Identify the blood parasite species.
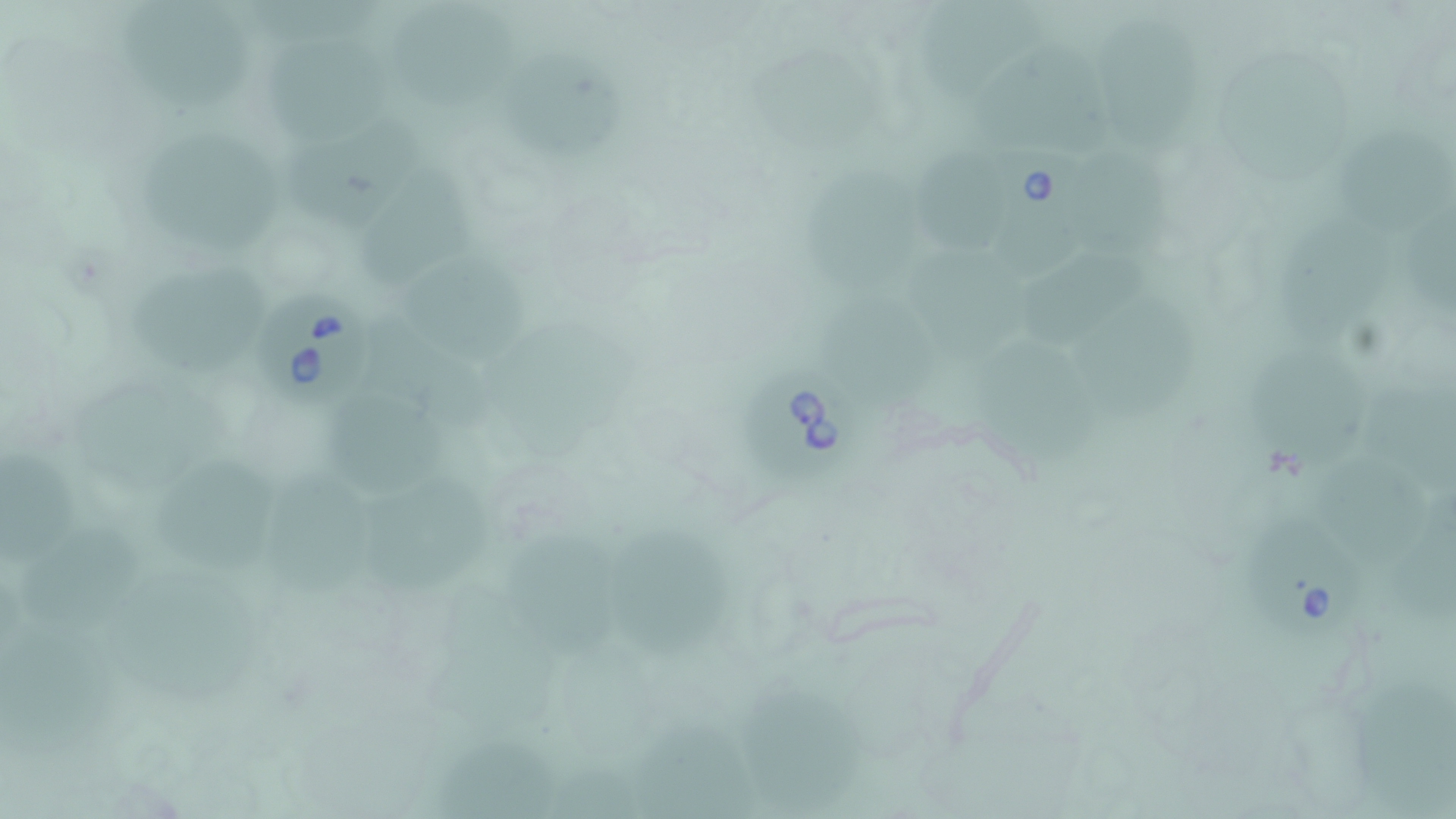
Babesia divergens.

Approximate bounding boxes as (x1,y1)-(x2,y2) corner pairs in pixels. Uninfected red blood cell locations: (252,0)-(383,58), (924,0)-(1044,107), (406,2)-(524,105), (118,5)-(263,111), (1107,19)-(1209,167), (991,39)-(1110,163), (265,41)-(391,139), (1228,50)-(1349,186), (760,54)-(883,160), (528,58)-(629,159), (287,113)-(425,229), (1345,119)-(1451,231), (141,131)-(287,249), (922,148)-(1023,253), (1086,152)-(1185,263), (359,153)-(476,279), (814,171)-(928,301), (1406,203)-(1456,325), (1276,212)-(1373,348), (914,239)-(1027,364), (421,251)-(536,365), (1022,253)-(1149,342), (133,271)-(276,371), (1079,291)-(1196,414), (822,295)-(940,412), (369,316)-(499,420), (500,320)-(645,467), (1248,338)-(1367,467), (992,345)-(1095,473), (76,375)-(209,499), (1370,380)-(1456,495), (342,397)-(456,498), (1318,435)-(1421,553), (1,443)-(86,573), (166,455)-(283,574), (268,472)-(383,596), (373,480)-(497,591), (1392,490)-(1456,623), (28,523)-(146,636), (629,527)-(736,671), (512,530)-(633,659), (127,572)-(267,696), (5,623)-(117,761), (1345,675)-(1456,818), (747,679)-(877,816), (637,719)-(749,816), (440,735)-(560,819), (548,754)-(639,818). Babesia divergens-infected red blood cell locations: (992,148)-(1095,279), (253,290)-(382,408), (744,358)-(855,481), (1252,510)-(1363,637). Light microscopy. Thin blood film. One field of a larger specimen. Captured at 1000x magnification. Image is 1456×819 pixels. May-Grünwald-Giemsa-stained preparation.